Locate every Babesia divergens-infected red blood cell.
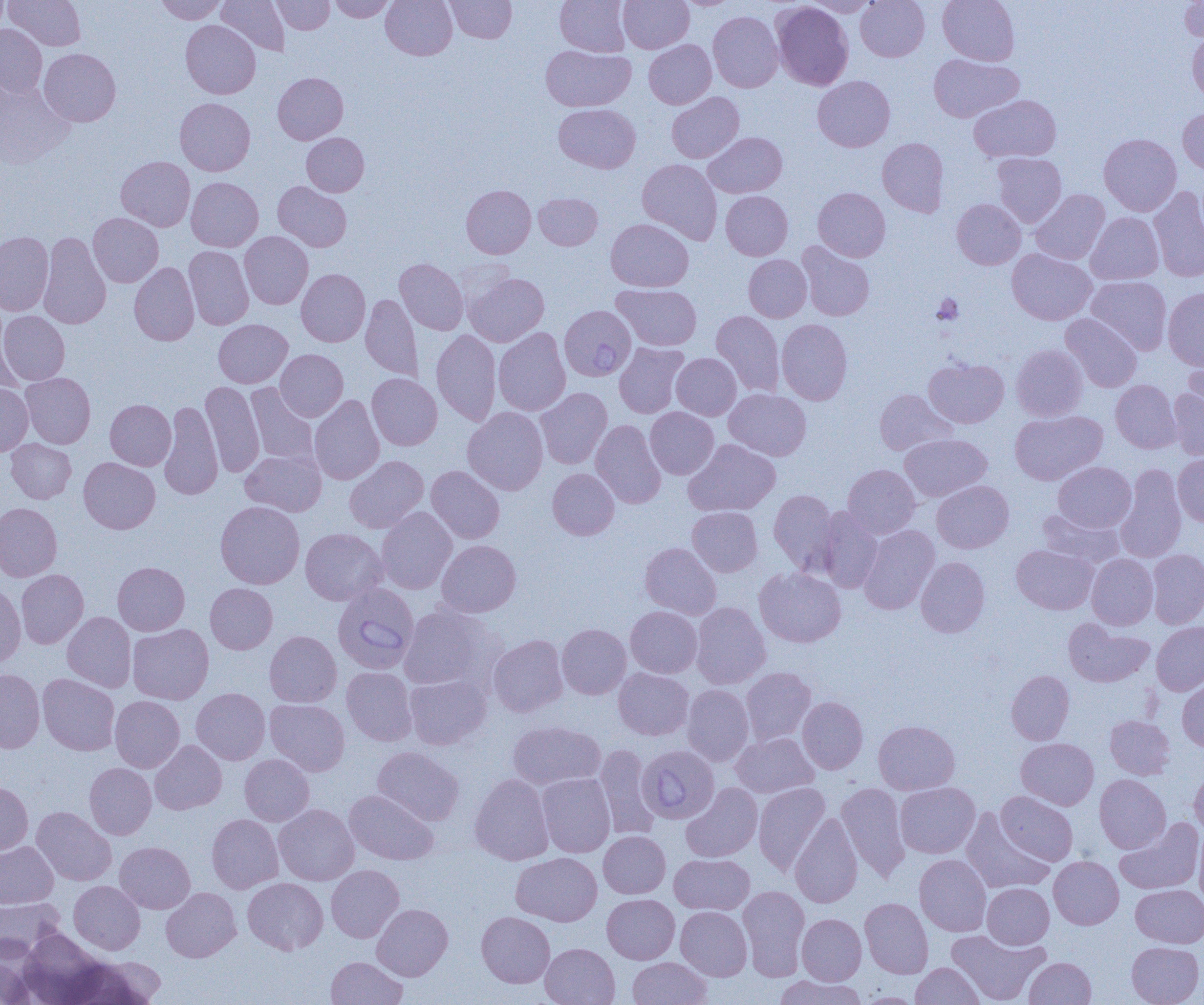

Approximate bounding boxes as (x1,y1)-(x2,y2) corner pairs in pixels.
Babesia divergens-infected red blood cells: (564,307)-(634,380), (333,583)-(419,674), (642,744)-(716,823).

slide-level diagnosis = Babesia divergens
magnification = 1000x
modality = optical microscopy
image size = 1204×1005 pixels
preparation = thin blood film
field of view = one of a larger specimen
uninfected red blood cell locations = approximate bounding boxes as (x1,y1)-(x2,y2) corner pairs in pixels: (0,0)-(11,33), (5,0)-(85,50), (156,0)-(227,24), (216,0)-(290,56), (272,0)-(334,34), (329,0)-(395,22), (381,0)-(457,60), (445,0)-(517,43), (556,0)-(630,56), (619,0)-(694,53), (674,0)-(741,10), (805,0)-(880,17), (856,0)-(930,61), (938,0)-(1019,66), (1180,0)-(1204,42), (772,2)-(853,90), (708,11)-(783,92), (181,20)-(260,98), (0,25)-(47,98), (1187,33)-(1204,102), (644,40)-(716,109), (541,45)-(635,111), (39,48)-(121,126), (929,54)-(1022,122), (273,72)-(348,144), (813,76)-(894,152), (0,81)-(74,169), (667,92)-(744,163), (969,95)-(1061,163), (175,98)-(255,175), (554,104)-(641,173), (1178,106)-(1204,174), (302,132)-(369,196), (703,132)-(787,198), (1098,133)-(1181,216), (877,138)-(949,217), (992,152)-(1066,227), (116,156)-(195,231), (637,159)-(722,245), (186,177)-(263,251), (273,181)-(352,251), (461,185)-(535,258), (1149,186)-(1204,282), (813,187)-(890,261), (1030,189)-(1109,265), (721,191)-(793,260), (534,193)-(602,250), (952,199)-(1026,269), (1085,212)-(1163,285), (88,213)-(163,287), (606,219)-(693,291), (0,231)-(54,315), (240,231)-(313,309), (39,232)-(111,329), (797,242)-(874,321), (184,246)-(254,329), (1007,248)-(1097,324), (743,255)-(812,322), (394,258)-(468,335), (129,262)-(199,345), (296,268)-(370,346), (464,272)-(549,346), (1086,276)-(1172,354), (612,284)-(701,350), (1163,288)-(1204,370), (361,293)-(422,381), (711,310)-(785,396), (0,311)-(70,385), (1060,314)-(1142,391), (213,319)-(292,388), (777,319)-(853,405), (0,322)-(23,398), (493,327)-(571,415), (431,330)-(501,426), (614,342)-(689,418), (1011,344)-(1087,421), (1184,344)-(1204,421), (275,349)-(348,421), (672,353)-(741,420), (924,358)-(1009,428), (21,373)-(96,448), (367,373)-(442,450), (1111,380)-(1181,453), (200,381)-(264,477), (0,383)-(33,456), (245,383)-(318,466), (535,387)-(612,469), (1168,388)-(1204,459), (724,389)-(811,460), (874,389)-(956,455), (309,395)-(385,485), (105,399)-(176,470), (159,400)-(223,500), (462,407)-(549,495), (645,407)-(718,479), (1010,411)-(1106,485), (590,420)-(666,508), (899,434)-(992,501), (6,439)-(76,503), (684,439)-(780,516), (241,448)-(326,516), (1173,454)-(1204,526), (344,456)-(429,533), (79,457)-(160,534), (1053,461)-(1136,532), (843,464)-(920,538), (426,465)-(505,543), (1115,465)-(1187,563), (547,468)-(619,540), (932,480)-(1014,553), (769,489)-(838,572), (215,501)-(305,589), (0,503)-(61,581), (376,507)-(457,594), (687,507)-(763,577), (815,507)-(883,593), (1037,509)-(1124,569), (858,525)-(939,614), (300,528)-(387,605), (437,539)-(521,617), (640,542)-(721,619), (1012,544)-(1098,614), (1147,549)-(1204,628), (1086,554)-(1158,629), (916,557)-(990,637), (113,562)-(189,635), (754,567)-(846,647), (16,569)-(88,648), (0,583)-(25,668), (205,583)-(277,654), (691,603)-(770,689), (399,604)-(500,691), (625,606)-(702,678), (62,612)-(136,692), (1064,617)-(1153,687), (1151,621)-(1204,695), (127,624)-(213,704), (557,624)-(631,699), (264,631)-(342,707), (489,634)-(567,717), (342,666)-(418,746), (741,667)-(816,745), (0,668)-(45,753), (614,668)-(693,740), (1006,670)-(1074,744), (404,673)-(491,749), (38,674)-(119,755), (1178,678)-(1204,752), (682,684)-(754,766), (191,688)-(270,764), (110,696)-(184,772), (797,696)-(868,774), (265,699)-(350,776), (1105,716)-(1174,779), (873,720)-(960,794), (507,721)-(605,790), (731,732)-(819,798), (1016,738)-(1099,809), (150,740)-(227,814), (594,744)-(659,839), (372,747)-(464,825), (240,754)-(314,825), (85,763)-(156,839), (1189,766)-(1204,837), (536,773)-(615,857), (469,774)-(554,865), (1094,774)-(1171,853), (0,781)-(33,857), (753,782)-(830,875), (895,782)-(980,858), (681,783)-(762,862), (837,783)-(910,881), (344,790)-(438,865), (996,791)-(1078,865), (274,804)-(359,885), (32,806)-(116,885), (961,809)-(1053,894), (790,813)-(863,907), (207,814)-(283,893), (1115,818)-(1204,894), (1193,826)-(1204,909), (598,830)-(670,898), (0,842)-(58,908), (115,842)-(195,913), (511,852)-(602,926), (670,854)-(754,915), (914,854)-(991,936), (1049,856)-(1124,929), (326,865)-(404,942), (243,878)-(328,954), (69,881)-(145,955), (982,883)-(1054,949), (1131,884)-(1204,947), (738,886)-(810,980), (161,887)-(241,962), (602,894)-(679,964), (0,897)-(64,957), (860,898)-(933,978), (372,903)-(453,980), (676,906)-(752,980), (476,911)-(555,987), (796,913)-(866,985), (18,929)-(108,1004), (946,929)-(1048,1004), (1126,942)-(1203,1005), (540,943)-(619,1005), (0,947)-(37,1005), (74,955)-(167,1003), (326,956)-(408,1005), (628,957)-(712,1005), (1024,957)-(1096,1005), (911,963)-(984,1004), (773,975)-(865,1005), (856,992)-(924,1004)
platelet locations = approximate bounding boxes as (x1,y1)-(x2,y2) corner pairs in pixels: (932,293)-(963,325)